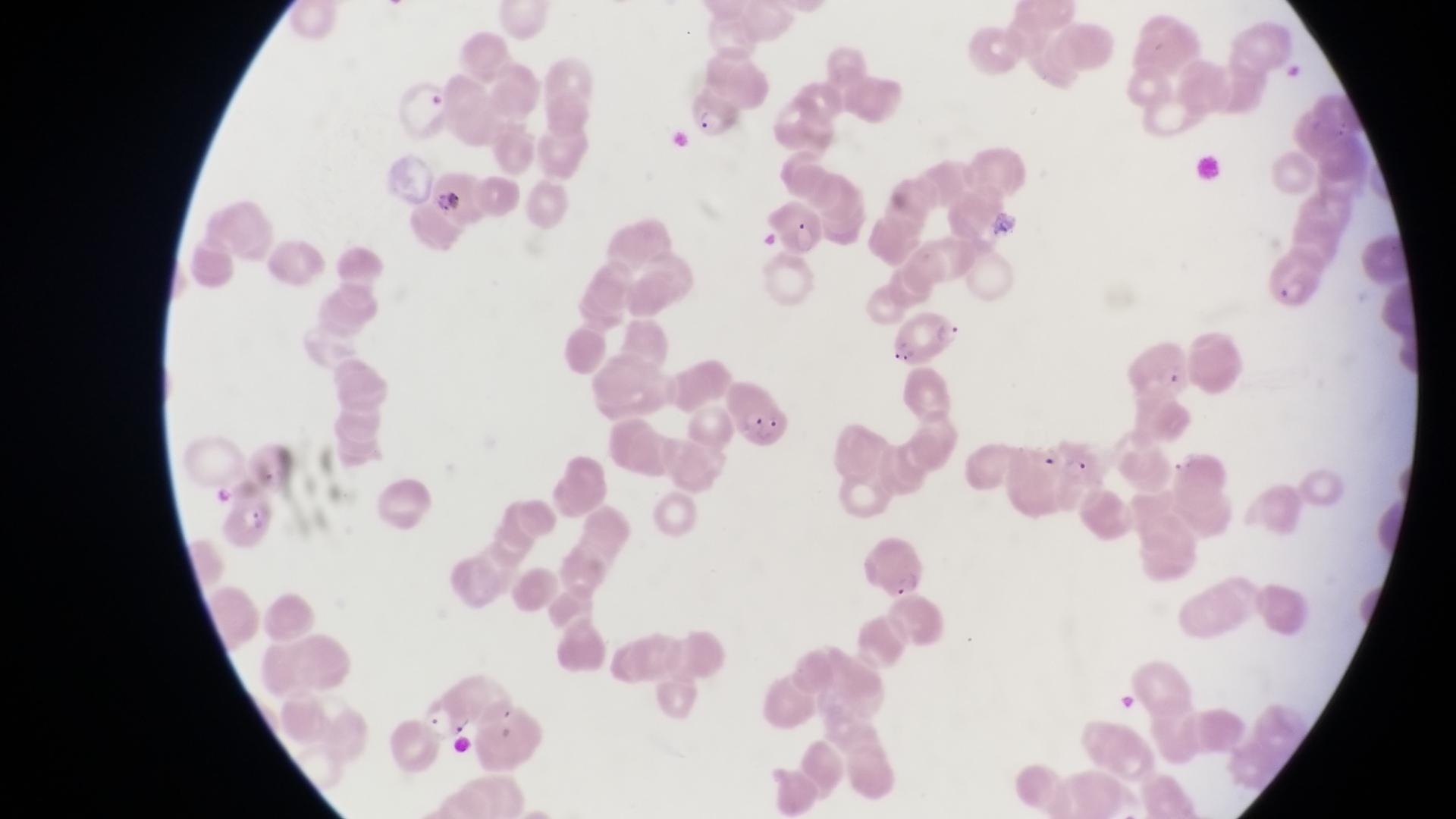

{
  "preparation": "thin blood film",
  "image_size": "1456×819 pixels",
  "parasitised_red_blood_cell_locations": "approximate bounding boxes as [left, top, right, bottom] in pixels: [686, 89, 736, 139], [770, 199, 825, 258], [1264, 243, 1327, 312], [893, 314, 969, 372], [721, 380, 795, 447]",
  "field_of_view": "single",
  "capture": "smartphone photograph through the eyepiece of an Olympus CX-23 microscope",
  "trophozoite_locations": "approximate bounding boxes as [left, top, right, bottom] in pixels: [1063, 455, 1097, 487]",
  "artifact_platelet_like_body_stain_precipitate_or_debris_locations": "approximate bounding boxes as [left, top, right, bottom] in pixels: [429, 184, 468, 217]",
  "magnification": "1000x",
  "country": "Uganda"
}